Identify the parasite.
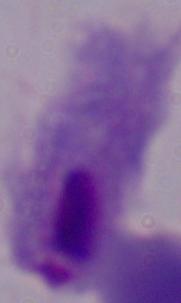
This is a trichomonad.

Summary:
  - Magnification: 1000x
  - Modality: photomicrograph